Assess this cell for malaria.
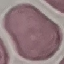
It is uninfected.

Summary:
  - Image type: automatically extracted cell patch, resized to 64 × 64 pixels
  - Capture: smartphone through the microscope eyepiece
  - Preparation: thin blood film
  - Stain: Giemsa